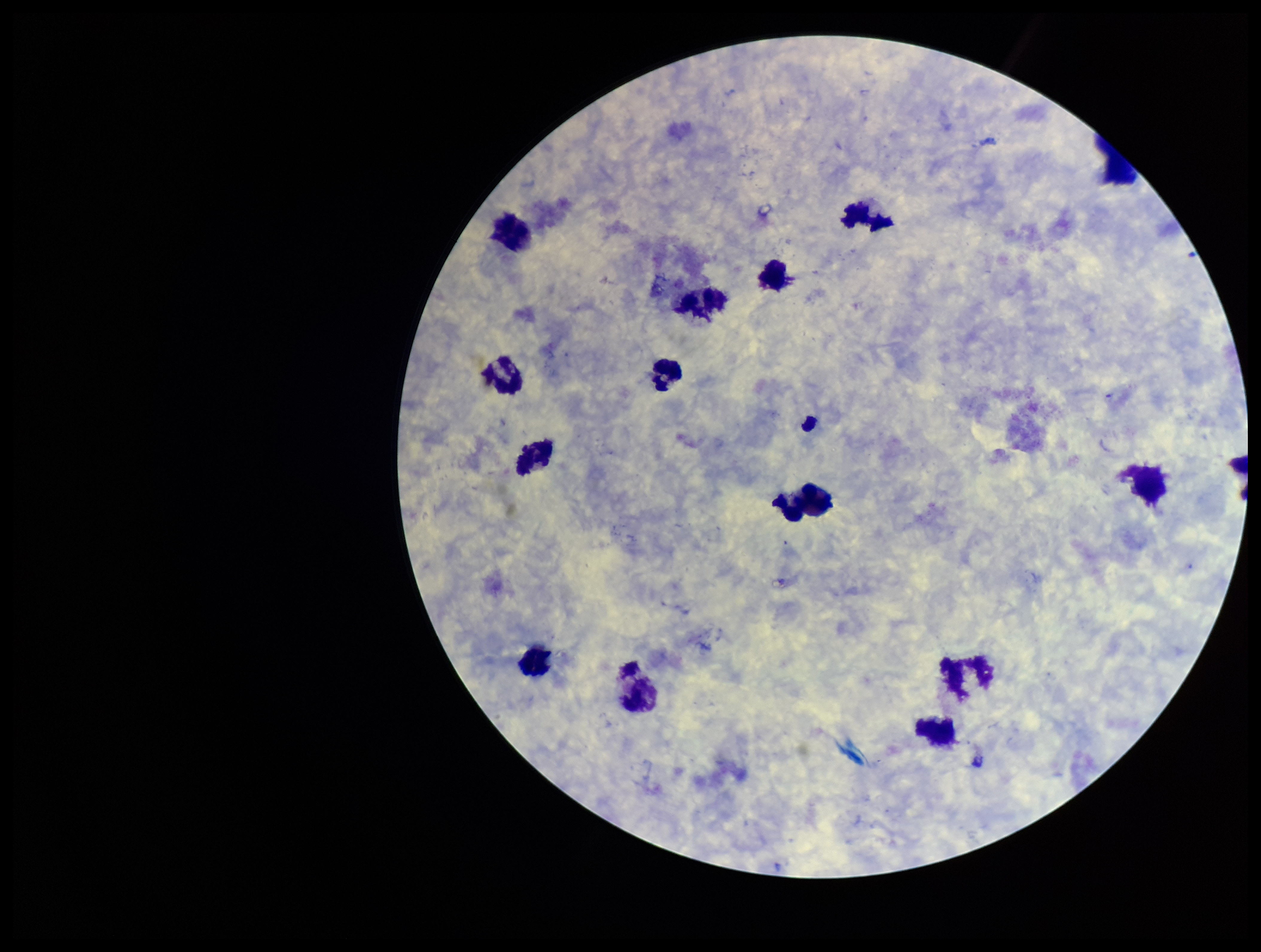 Giemsa stain. One field from this slide. Leukocyte count: 14. Parasite count: 0. Smartphone photograph taken through the eyepiece of a microscope. Image is 1261×952 pixels. Patient malaria status: negative. Preparation: thick blood smear. Plasmodium parasites: none seen.